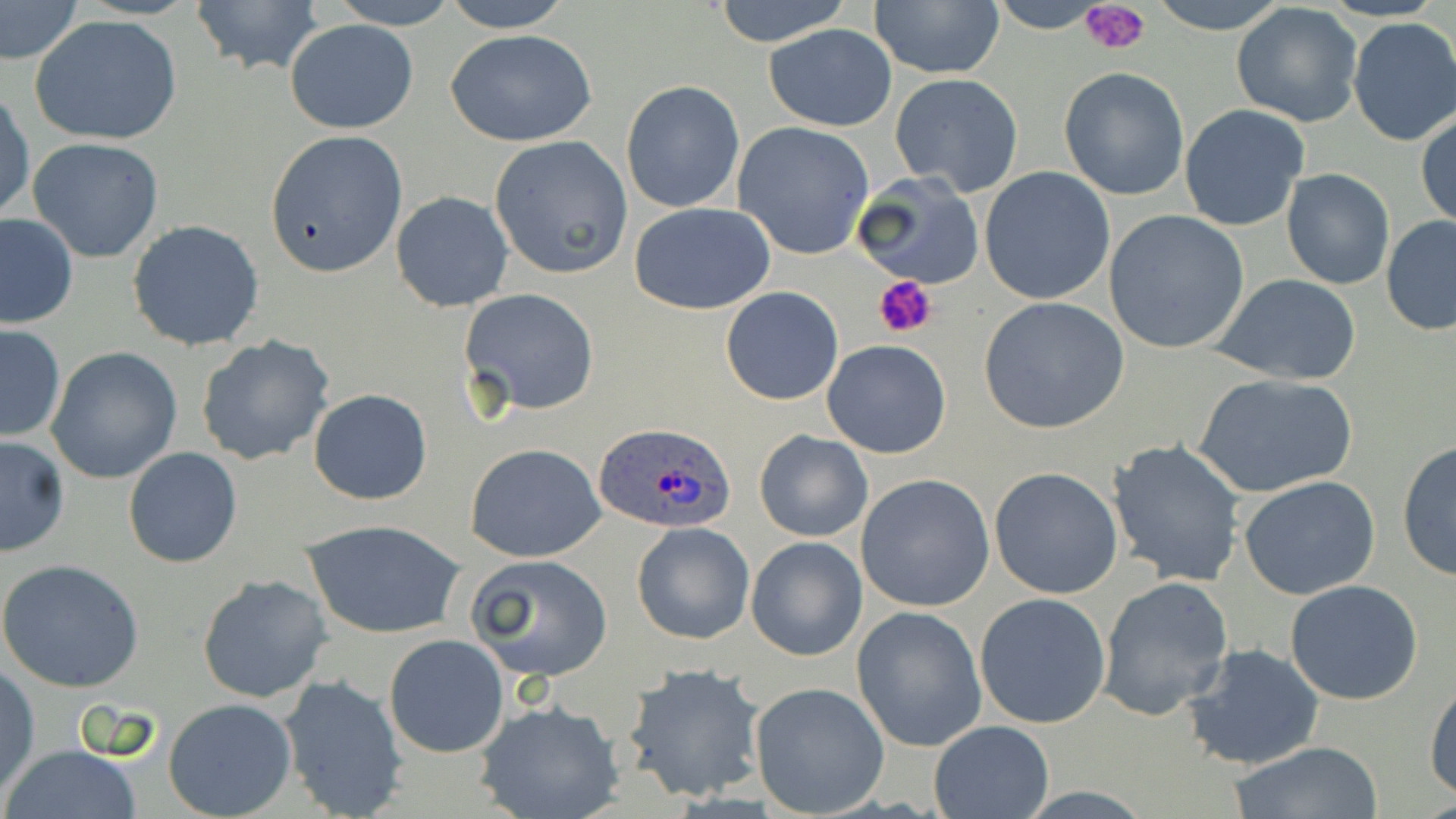

Summary:
  - Coordinate format: approximate bounding boxes as (x1, y1, x2, y2) in pixels
  - Plasmodium ovale-infected red blood cell locations: (596, 422, 736, 533)
  - Uninfected red blood cell locations: (0, 0, 83, 66), (189, 0, 326, 80), (327, 0, 464, 28), (437, 0, 575, 33), (712, 0, 854, 49), (1147, 0, 1291, 34), (868, 2, 1004, 79), (1231, 2, 1364, 128), (29, 14, 185, 146), (1347, 17, 1456, 146), (284, 18, 419, 134), (765, 22, 898, 131), (446, 28, 597, 146), (1058, 66, 1191, 200), (889, 73, 1023, 197), (621, 80, 745, 213), (0, 88, 35, 226), (1179, 104, 1310, 231), (1416, 109, 1455, 231), (732, 121, 876, 260), (264, 129, 407, 279), (28, 136, 165, 262), (489, 136, 634, 278), (979, 166, 1115, 306), (1281, 168, 1396, 291), (855, 173, 985, 290), (390, 191, 515, 312), (628, 201, 776, 315), (1103, 210, 1250, 353), (0, 213, 78, 328), (1381, 214, 1456, 335), (127, 220, 265, 353), (1213, 274, 1362, 386), (720, 286, 845, 405), (460, 288, 601, 417), (979, 297, 1132, 436), (0, 325, 67, 443), (195, 334, 336, 467), (821, 340, 950, 459), (46, 346, 183, 485), (1193, 373, 1359, 497), (308, 387, 433, 504), (755, 430, 872, 543), (0, 435, 70, 558), (1106, 439, 1246, 586), (1396, 441, 1455, 579), (464, 443, 607, 564), (123, 447, 243, 568), (989, 467, 1123, 599), (855, 473, 996, 613), (1239, 475, 1382, 600), (302, 518, 465, 641), (631, 521, 756, 644), (745, 537, 867, 661), (465, 553, 615, 683), (0, 559, 146, 692), (196, 573, 334, 704), (1097, 576, 1234, 720), (1284, 579, 1426, 703), (974, 592, 1111, 729), (851, 606, 987, 751), (384, 634, 509, 757), (1186, 644, 1324, 770), (621, 663, 767, 803), (0, 665, 39, 797), (277, 674, 408, 817), (1425, 676, 1456, 803), (749, 682, 890, 816), (163, 699, 298, 819), (473, 700, 624, 819), (928, 720, 1054, 818), (1228, 741, 1386, 819), (2, 745, 143, 819)
  - Platelet locations: (1078, 0, 1151, 55), (874, 275, 938, 340)
  - Slide-level diagnosis: Plasmodium ovale
  - Image size: 1456×819 pixels
  - Preparation: thin blood film
  - Stain: May-Grünwald-Giemsa
  - Field of view: one of a larger specimen
  - Magnification: 1000x
  - Modality: light microscopy